Identify the parasite.
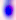
This is Toxoplasma gondii.

Micrograph. Captured at 400x magnification.